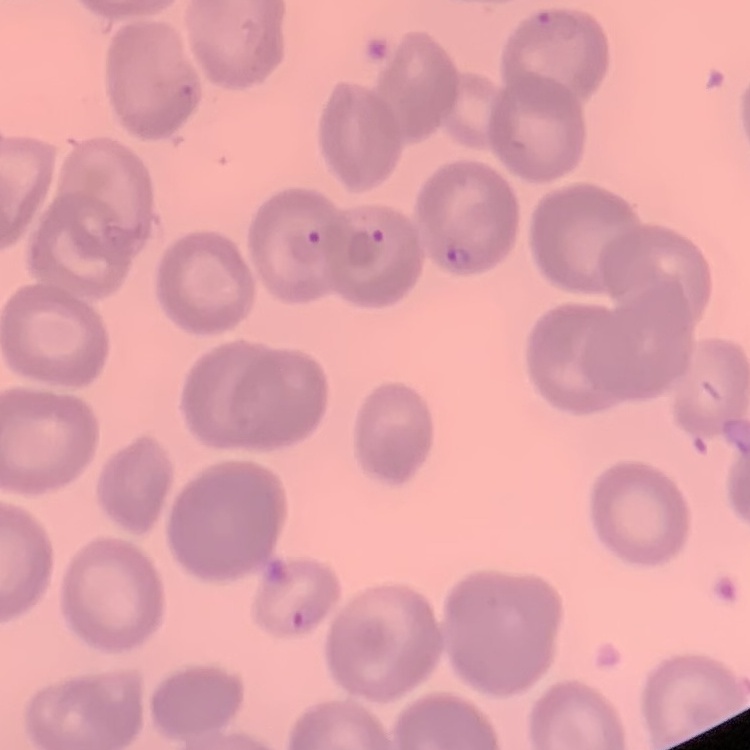
Summary:
  - Red blood cell morphology: no rouleaux formation
  - Preparation: thin blood smear
  - Image type: one tile cut from a larger photomicrograph
  - Stain: Field's or Giemsa